Assess this cell for malaria.
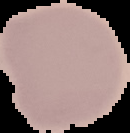
Uninfected.

From a thin blood smear. Image is 130×133 pixels. Cell region segmented out of the field of view; the surrounding area is masked to black.